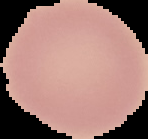
Image is 148×139 pixels. Cell region segmented out of the field of view; the surrounding area is masked to black. Result: no malaria parasites detected. From a thin blood smear.